Name the parasite shown.
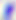

Toxoplasma gondii.

Summary:
  - Modality: micrograph
  - Magnification: 400x